Assess this cell for malaria.
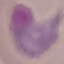

Parasitized.

Automatically extracted cell patch, resized to 64 × 64 pixels. Acquired by smartphone through the microscope eyepiece. Giemsa-stained preparation. Thin blood smear.